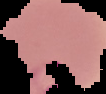
Image is 106×94 pixels. From a thin blood film. Segmented cell region on a black background. Result: Plasmodium parasites detected.